Assess the morphology of the red blood cells.
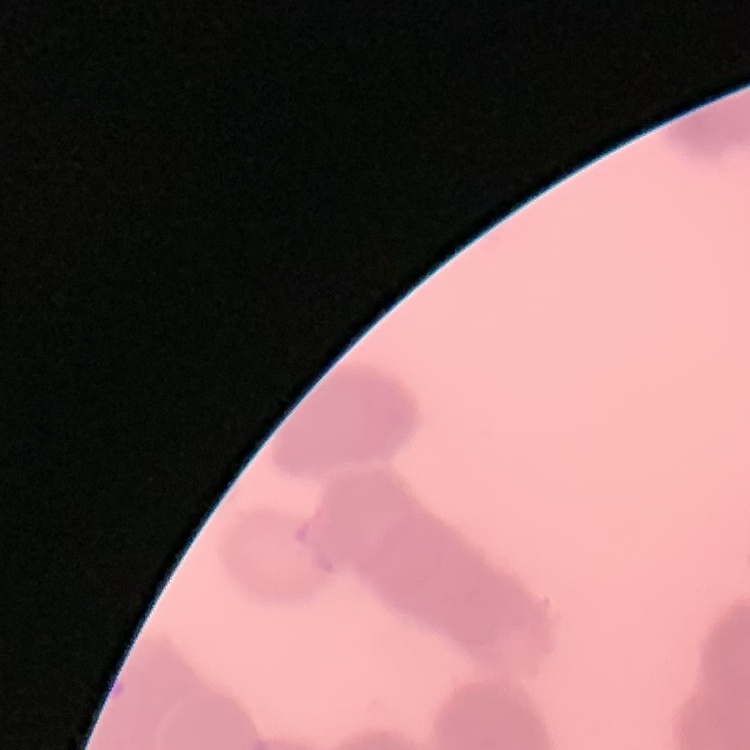
Rouleaux formation.

One tile cut from a larger photomicrograph. Thin peripheral smear. Stained with either Field's or Giemsa.